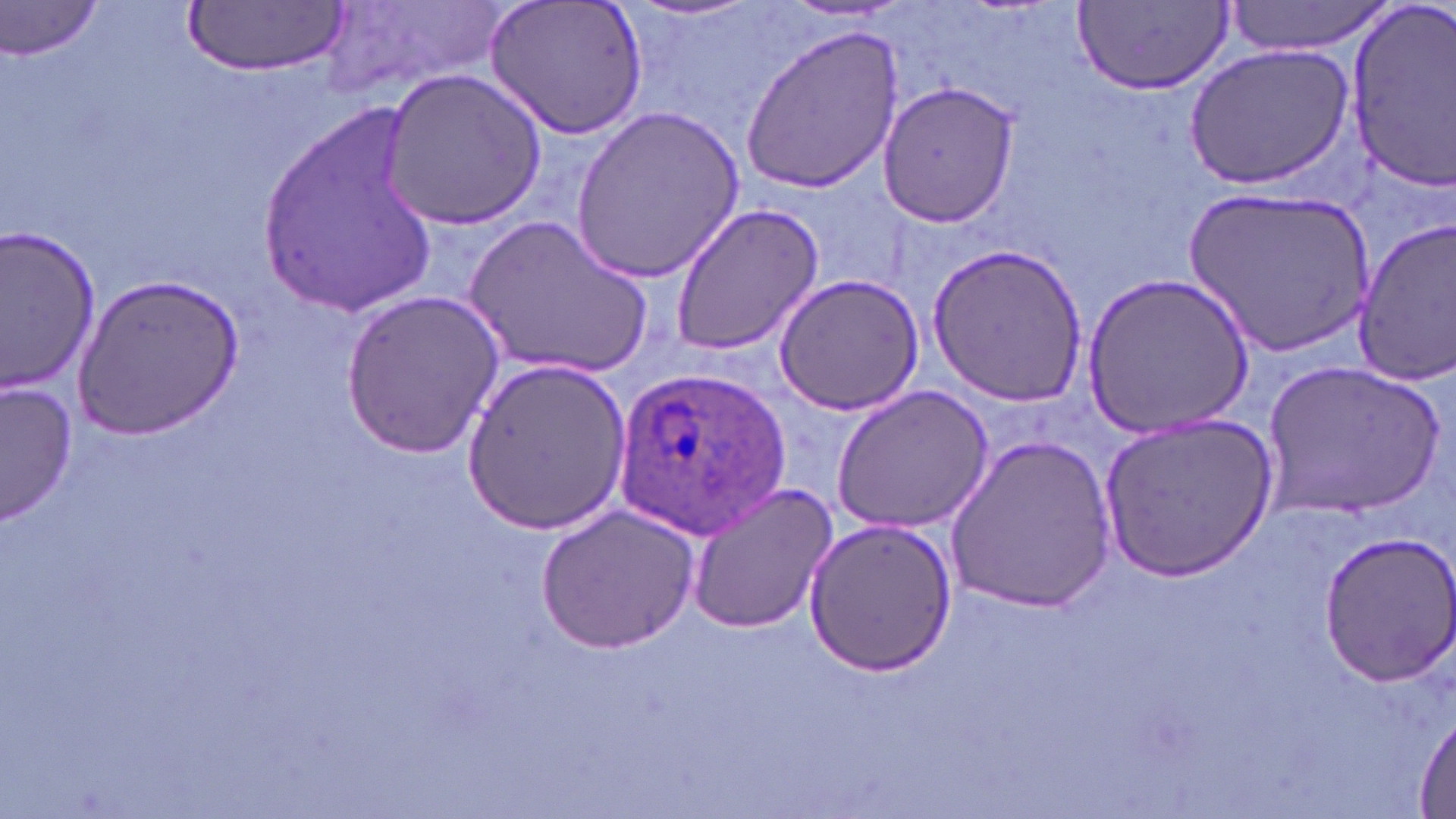 Approximate bounding boxes as named x1/y1/x2/y2 corners in pixels. Uninfected red blood cell locations: (x1=322, y1=0, x2=509, y2=102), (x1=484, y1=0, x2=649, y2=139), (x1=628, y1=0, x2=764, y2=25), (x1=1223, y1=0, x2=1397, y2=57), (x1=1, y1=1, x2=110, y2=62), (x1=1072, y1=1, x2=1234, y2=93), (x1=182, y1=2, x2=347, y2=77), (x1=1339, y1=5, x2=1456, y2=191), (x1=740, y1=25, x2=907, y2=194), (x1=1180, y1=40, x2=1357, y2=192), (x1=378, y1=67, x2=548, y2=230), (x1=876, y1=80, x2=1021, y2=226), (x1=569, y1=102, x2=746, y2=283), (x1=256, y1=103, x2=444, y2=311), (x1=1182, y1=183, x2=1374, y2=360), (x1=669, y1=202, x2=825, y2=356), (x1=466, y1=213, x2=655, y2=383), (x1=1349, y1=213, x2=1456, y2=385), (x1=0, y1=226, x2=100, y2=392), (x1=926, y1=243, x2=1090, y2=407), (x1=1084, y1=270, x2=1254, y2=442), (x1=73, y1=272, x2=244, y2=441), (x1=772, y1=273, x2=926, y2=416), (x1=339, y1=289, x2=504, y2=459), (x1=460, y1=356, x2=633, y2=533), (x1=1262, y1=360, x2=1442, y2=518), (x1=2, y1=381, x2=78, y2=526), (x1=831, y1=383, x2=994, y2=534), (x1=1096, y1=412, x2=1275, y2=582), (x1=944, y1=432, x2=1116, y2=616), (x1=684, y1=483, x2=840, y2=635), (x1=536, y1=504, x2=701, y2=655), (x1=801, y1=517, x2=958, y2=677), (x1=1315, y1=530, x2=1456, y2=688), (x1=1413, y1=710, x2=1456, y2=816). Plasmodium ovale-infected red blood cell locations: (x1=615, y1=362, x2=793, y2=539). Slide-level diagnosis: Plasmodium ovale. Thin blood film. May-Grünwald-Giemsa-stained preparation. Captured at 1000x magnification. Image is 1456×819 pixels. One field of a larger specimen. Optical microscopy.